Give the extent of all white blood cells.
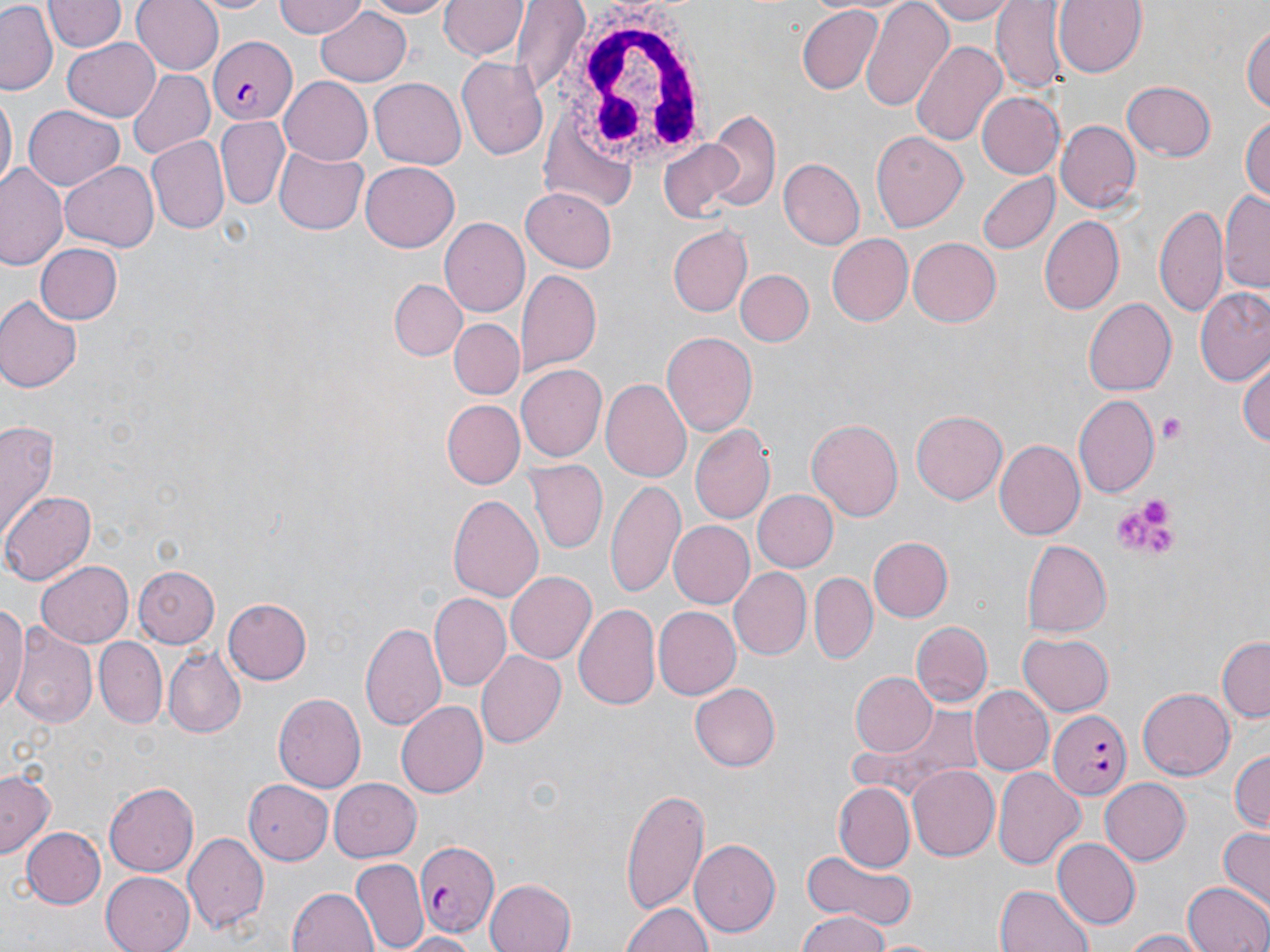
Approximate bounding boxes as (x1, y1, x2, y2) in pixels.
White blood cells: (560, 9, 716, 171).

slide_level_diagnosis: Plasmodium falciparum
magnification: 1000x
preparation: thin blood film
field_of_view: single
stain: May-Grünwald-Giemsa
plasmodium_falciparum_infected_red_blood_cell_locations: 'approximate bounding boxes as (x1, y1, x2, y2) in pixels: (211, 35, 297, 125), (1050, 711, 1131, 796), (411, 838, 498, 937)'
image_size: 1270×952 pixels
uninfected_red_blood_cell_locations: 'approximate bounding boxes as (x1, y1, x2, y2) in pixels: (46, 0, 124, 54), (132, 0, 224, 75), (190, 0, 278, 15), (275, 0, 368, 39), (352, 0, 459, 18), (440, 0, 528, 62), (859, 0, 953, 110), (919, 0, 1015, 24), (1054, 0, 1147, 77), (993, 1, 1069, 93), (1, 3, 60, 97), (513, 3, 589, 95), (312, 6, 413, 88), (795, 6, 884, 95), (1244, 20, 1270, 120), (909, 38, 1008, 151), (61, 39, 158, 120), (456, 54, 551, 163), (126, 67, 214, 160), (278, 77, 372, 165), (370, 78, 465, 169), (1119, 80, 1215, 163), (0, 90, 16, 193), (976, 92, 1066, 179), (24, 106, 124, 190), (702, 111, 780, 211), (1241, 113, 1270, 207), (216, 117, 289, 208), (1058, 119, 1141, 213), (870, 130, 968, 233), (658, 137, 749, 222), (146, 138, 228, 234), (274, 146, 369, 235), (778, 159, 864, 250), (1, 162, 69, 270), (59, 162, 159, 251), (361, 163, 459, 251), (976, 170, 1059, 255), (521, 187, 619, 271), (1219, 188, 1270, 292), (1155, 205, 1228, 319), (1041, 216, 1124, 313), (438, 217, 530, 317), (666, 225, 751, 316), (825, 234, 912, 326), (909, 237, 1001, 328), (35, 243, 124, 325), (734, 270, 813, 347), (518, 271, 603, 373), (390, 278, 466, 360), (1195, 284, 1270, 388), (0, 293, 81, 395), (1084, 296, 1176, 396), (449, 317, 524, 399), (661, 331, 758, 436), (1238, 352, 1270, 452), (516, 361, 607, 459), (600, 377, 691, 481), (1075, 396, 1159, 496), (441, 399, 524, 489), (911, 409, 1007, 505), (1, 417, 60, 541), (806, 418, 905, 522), (691, 425, 775, 524), (994, 438, 1085, 541), (525, 460, 608, 552), (607, 477, 685, 599), (752, 489, 837, 572), (4, 490, 96, 583), (449, 493, 544, 605), (668, 520, 755, 608), (868, 536, 954, 622), (1022, 540, 1111, 636), (36, 559, 133, 648), (133, 565, 220, 646), (728, 566, 812, 661), (504, 571, 595, 664), (811, 572, 877, 660), (428, 593, 511, 693), (0, 596, 28, 718), (221, 596, 312, 686), (574, 602, 662, 713), (654, 607, 740, 700), (361, 619, 448, 733), (912, 620, 991, 708), (10, 627, 97, 731), (1018, 633, 1114, 716), (93, 637, 167, 727), (1216, 637, 1270, 720), (163, 644, 245, 739), (478, 651, 566, 748), (850, 672, 938, 757), (690, 682, 780, 772), (968, 685, 1052, 775), (1138, 688, 1234, 781), (274, 692, 366, 791), (396, 700, 488, 799), (840, 705, 994, 803), (1229, 748, 1269, 836), (908, 766, 999, 863), (1, 768, 57, 860), (994, 768, 1085, 871), (327, 778, 419, 862), (1099, 778, 1191, 866), (243, 779, 333, 866), (105, 783, 199, 875), (834, 784, 914, 868), (620, 787, 710, 913), (22, 827, 107, 909), (1218, 827, 1270, 908), (184, 833, 270, 934), (1053, 837, 1139, 930), (689, 838, 781, 937), (798, 851, 919, 931), (354, 857, 428, 952), (100, 870, 196, 952), (484, 877, 578, 952), (1182, 880, 1270, 952), (993, 883, 1096, 952), (288, 887, 378, 952), (621, 898, 714, 952), (793, 913, 895, 952), (1119, 928, 1213, 951), (392, 931, 483, 951)'
modality: light microscopy
platelet_locations: 'approximate bounding boxes as (x1, y1, x2, y2) in pixels: (1158, 413, 1188, 447), (1140, 496, 1170, 529), (1115, 516, 1150, 550), (1142, 527, 1179, 556)'